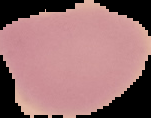

Summary:
  - Preparation: thin blood smear
  - Image size: 151×118 pixels
  - Result: negative for malaria parasites
  - Image type: cell region segmented out of the field of view; surrounding area masked to black